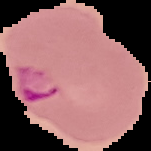
Cell region segmented out of the field of view; the surrounding area is masked to black. Image is 151×151 pixels. From a thin blood smear. Result: malaria parasites identified.